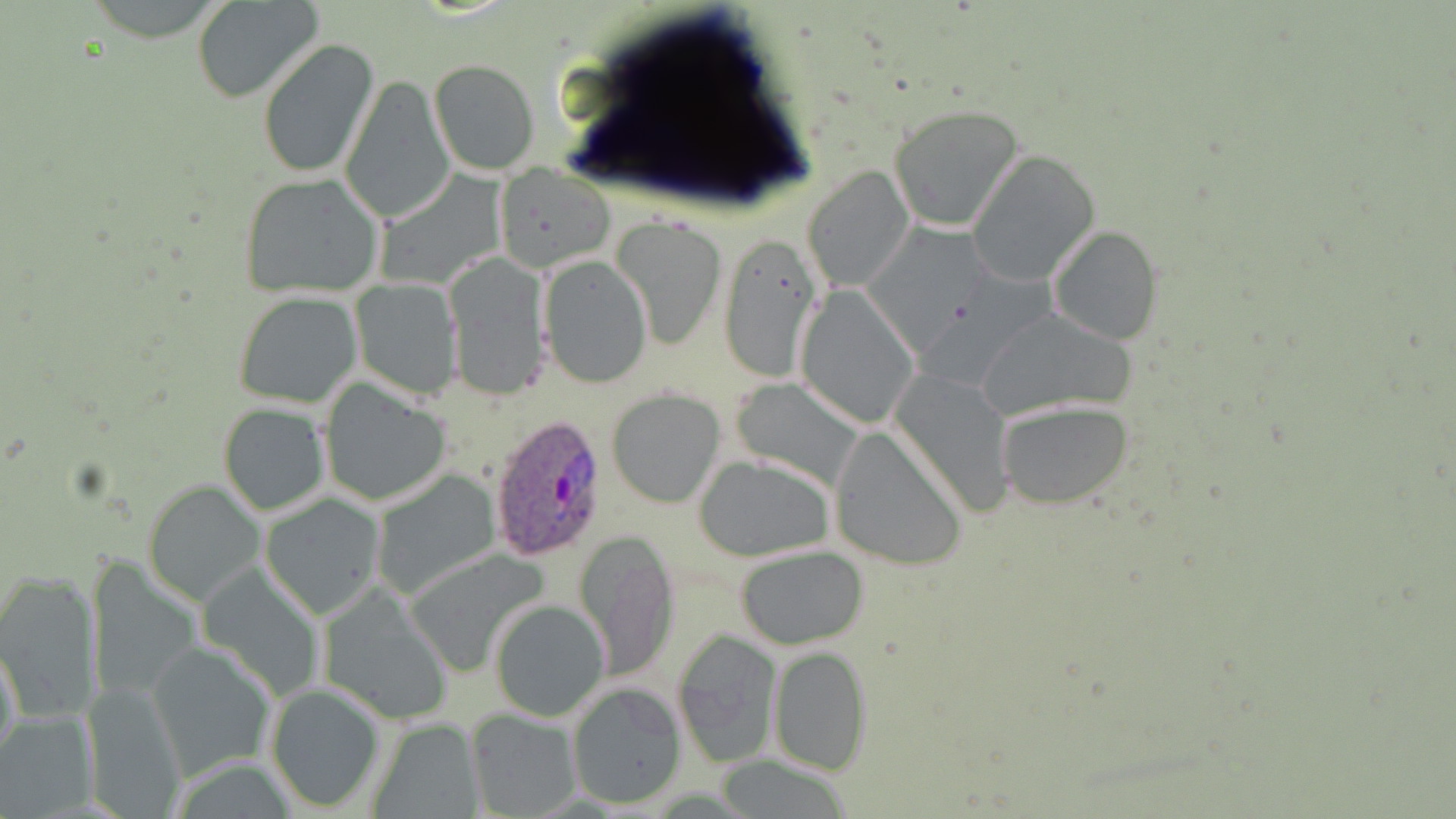

Approximate bounding boxes as (x1, y1, x2, y2) in pixels. Uninfected red blood cell locations: (194, 0, 325, 104), (258, 38, 379, 178), (428, 60, 539, 174), (338, 71, 455, 224), (889, 104, 1027, 231), (967, 150, 1101, 288), (496, 164, 613, 272), (802, 167, 913, 294), (239, 173, 384, 299), (611, 214, 730, 352), (859, 219, 989, 349), (1048, 226, 1164, 345), (718, 231, 824, 384), (445, 251, 549, 399), (540, 254, 650, 389), (351, 278, 460, 397), (796, 287, 922, 427), (233, 289, 363, 409), (972, 305, 1137, 422), (890, 368, 1016, 518), (728, 375, 871, 493), (318, 380, 452, 507), (608, 389, 726, 507), (995, 401, 1134, 511), (218, 403, 330, 517), (828, 427, 969, 571), (693, 454, 836, 561), (370, 468, 502, 599), (145, 480, 265, 607), (260, 492, 384, 619), (576, 529, 679, 682), (735, 546, 870, 649), (404, 548, 553, 674), (86, 557, 202, 705), (0, 573, 101, 721), (318, 587, 455, 725), (487, 598, 610, 722), (673, 629, 780, 767), (0, 639, 21, 773), (147, 640, 276, 780), (769, 645, 873, 775), (265, 681, 384, 813), (566, 682, 687, 809), (82, 683, 185, 817), (467, 709, 580, 818), (0, 710, 96, 815), (365, 716, 485, 818). Plasmodium ovale-infected red blood cell locations: (487, 415, 609, 562). Slide-level diagnosis: Plasmodium ovale. Captured at 1000x magnification. Single field of view. Thin blood smear. Image is 1456×819 pixels. Optical microscopy. May-Grünwald-Giemsa-stained preparation.